Report the malaria status.
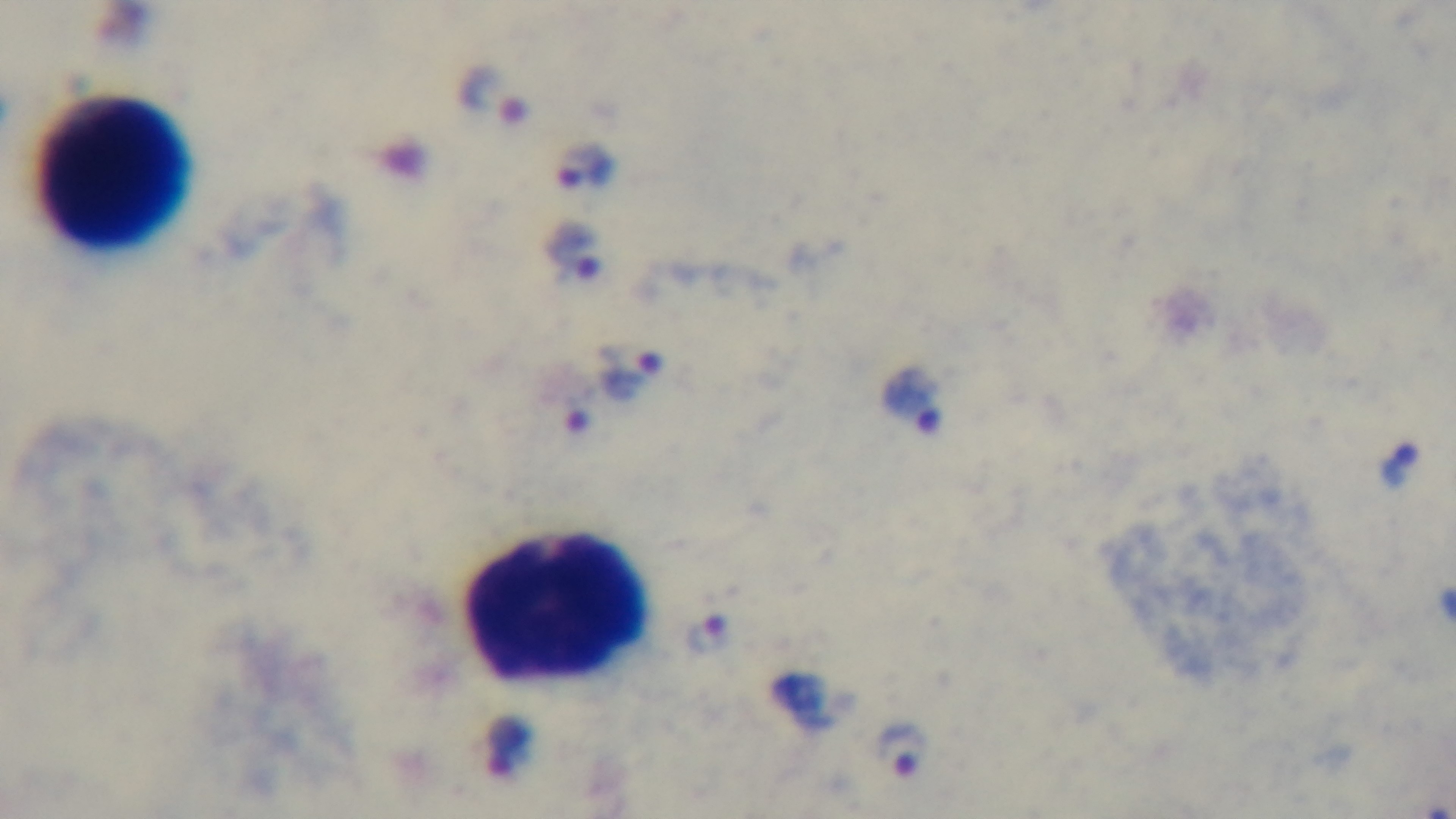
Positive.

capture = mounted 4K digital camera
objective = 100x oil immersion
modality = light microscopy
stain = Giemsa
preparation = thick blood film
field of view = single